Assess this cell for malaria.
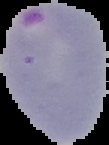

Parasitized.

Image is 109×145 pixels. From a thin blood film. Cell region segmented out of the field of view; the surrounding area is masked to black.